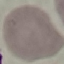 Result: no malaria parasites detected. Photographed with a smartphone camera at the microscope eyepiece. Thin smear of blood. Giemsa stain. Cell patch, automatically extracted from a larger field of view and resized to 64 × 64 pixels.